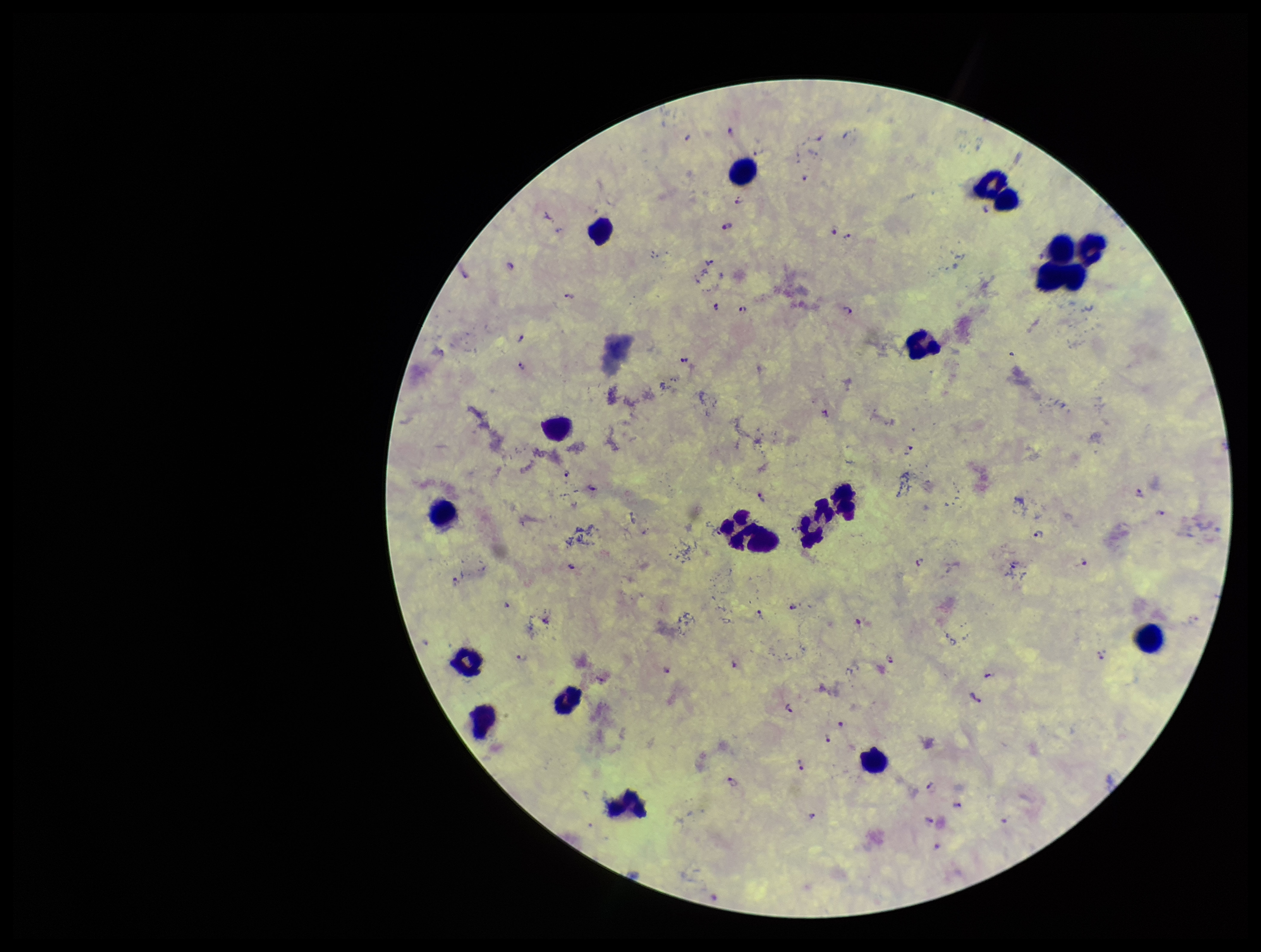
Summary:
  - Stain: Giemsa
  - Patient malaria status: positive
  - Image size: 1261×952 pixels
  - Preparation: thick blood smear
  - Plasmodium parasites: identified
  - Capture: smartphone photograph through the microscope eyepiece
  - Species reported for this patient: Plasmodium falciparum
  - Leukocyte count: 18
  - Parasite count: 53
  - Field of view: one from this slide